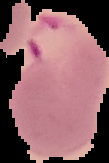
Summary:
  - Image size: 109×163 pixels
  - Result: Plasmodium parasites identified
  - Image type: cell region segmented out of the field of view; surrounding area masked to black
  - Preparation: thin blood film